Report the malaria status of this cell.
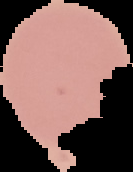

Uninfected.

Segmented cell region on a black background. From a thin blood film. Image is 133×172 pixels.